State the blood parasite species.
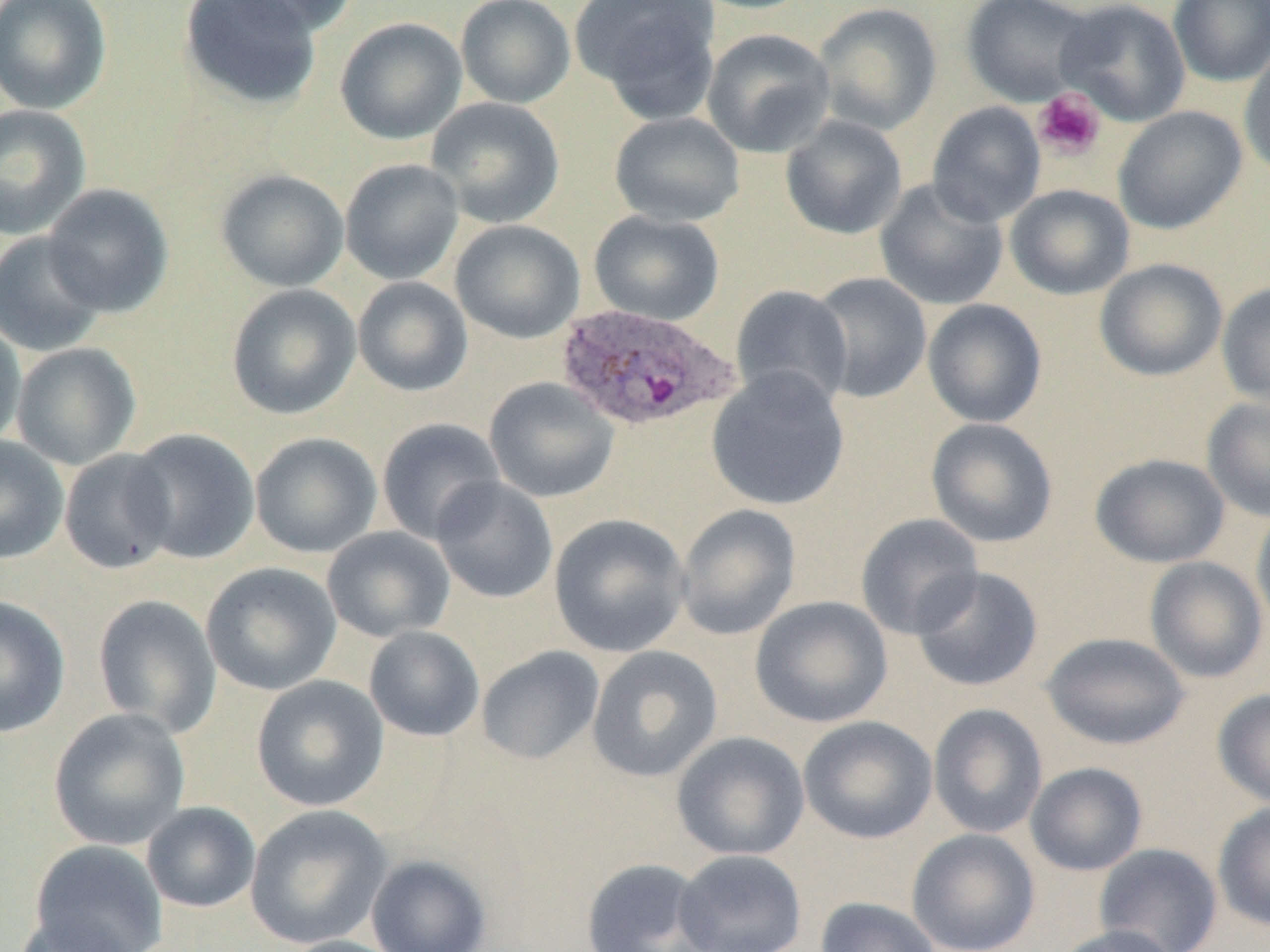
Plasmodium ovale.

{
  "preparation": "thin blood smear",
  "magnification": "1000x",
  "uninfected_red_blood_cell_locations": "approximate bounding boxes as (x1,y1)-(x2,y2) corner pairs in pixels: (0,0)-(112,115), (179,0)-(321,110), (217,0)-(360,36), (571,0)-(722,117), (688,0)-(818,14), (961,0)-(1097,107), (1056,0)-(1191,127), (1168,0)-(1270,87), (455,1)-(575,108), (812,2)-(943,136), (334,17)-(467,145), (701,28)-(835,158), (1239,44)-(1270,181), (426,97)-(565,228), (927,101)-(1046,227), (0,104)-(92,240), (1113,106)-(1247,234), (609,112)-(745,227), (780,114)-(907,240), (340,159)-(464,285), (216,169)-(349,292), (874,178)-(1009,311), (41,184)-(173,317), (1004,184)-(1135,300), (588,210)-(724,325), (450,219)-(585,343), (0,231)-(107,357), (1094,258)-(1227,381), (809,272)-(932,403), (352,277)-(473,397), (1216,281)-(1270,409), (226,284)-(362,420), (730,284)-(853,410), (922,298)-(1047,428), (0,317)-(26,451), (11,342)-(141,470), (706,366)-(850,511), (484,377)-(619,503), (1201,396)-(1270,522), (377,417)-(506,544), (925,417)-(1058,548), (124,428)-(260,564), (250,432)-(382,558), (0,435)-(69,565), (59,448)-(178,574), (1090,453)-(1231,568), (430,476)-(559,604), (675,503)-(801,641), (1250,507)-(1270,636), (549,512)-(691,658), (855,513)-(985,639), (322,526)-(455,642), (1144,557)-(1268,683), (201,562)-(342,695), (911,566)-(1044,692), (92,593)-(222,737), (0,595)-(70,738), (750,595)-(893,728), (364,626)-(485,742), (1041,632)-(1190,750), (586,645)-(723,783), (476,646)-(604,765), (251,674)-(389,811), (1212,688)-(1270,808), (928,704)-(1048,839), (48,707)-(191,851), (798,716)-(937,843), (671,731)-(810,861), (1025,762)-(1148,876), (141,801)-(261,913), (1213,801)-(1270,931), (244,805)-(393,949), (907,828)-(1040,952), (30,839)-(168,951), (1093,843)-(1223,952), (673,848)-(808,951), (366,854)-(492,952), (580,858)-(715,952), (815,896)-(942,952), (12,914)-(137,952), (1050,924)-(1182,952), (279,935)-(408,952)",
  "plasmodium_ovale_infected_red_blood_cell_locations": "approximate bounding boxes as (x1,y1)-(x2,y2) corner pairs in pixels: (554,302)-(740,432)",
  "platelet_locations": "approximate bounding boxes as (x1,y1)-(x2,y2) corner pairs in pixels: (1032,88)-(1106,161)",
  "field_of_view": "single",
  "modality": "light microscopy",
  "image_size": "1270×952 pixels"
}